Classify this cell by malaria status.
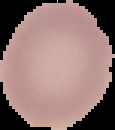

It is uninfected.

Summary:
  - Image type: segmented cell region on a black background
  - Image size: 115×130 pixels
  - Preparation: thin blood film